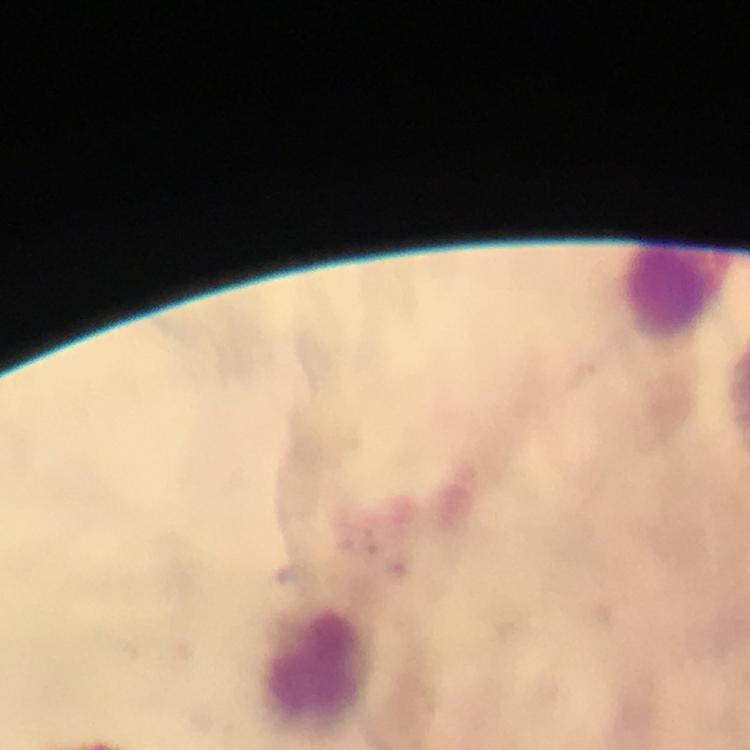

leukocyte_locations: 'approximate centers as (x, y) in pixels: (677, 291), (317, 664)'
capture: smartphone photograph through a microscope
immersion_oil: applied
stain: Giemsa
preparation: thick blood smear
image_size: 750×750 pixels
context: from a malaria diagnostic workup
cropped_from: a single field of view
plasmodium_parasites: none seen
magnification: 100x